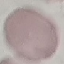 Malaria status: uninfected. Giemsa-stained preparation. Thin blood film. Acquired by smartphone through the microscope eyepiece. Automatically extracted cell patch, resized to 64 × 64 pixels.